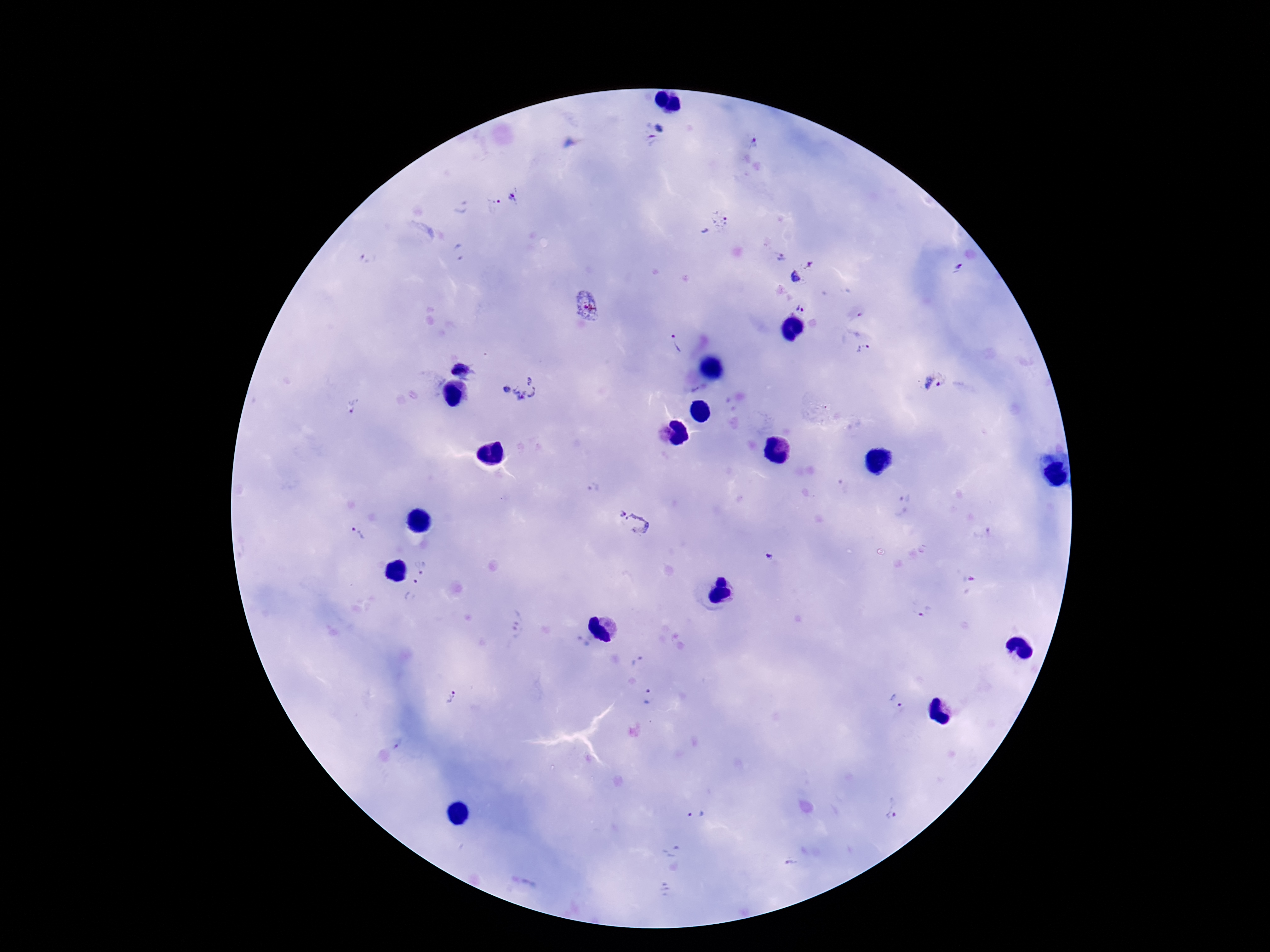
Approximate object centers, in pixels from the top-left corner.
Summary:
  - Plasmodium parasite locations: (x=658, y=128), (x=753, y=140), (x=652, y=141), (x=516, y=196), (x=493, y=204), (x=713, y=224), (x=457, y=253), (x=367, y=258), (x=781, y=258), (x=804, y=274), (x=586, y=303), (x=799, y=308), (x=675, y=344), (x=864, y=350), (x=462, y=368), (x=932, y=380), (x=518, y=388), (x=355, y=405), (x=620, y=513), (x=640, y=523), (x=358, y=535), (x=770, y=558), (x=421, y=564), (x=412, y=590), (x=924, y=611), (x=516, y=626), (x=649, y=697), (x=451, y=699), (x=895, y=700), (x=893, y=808), (x=695, y=814), (x=791, y=864)
  - Image size: 1270×952 pixels
  - Magnification: 100x
  - Patient malaria status: infected
  - Field of view: one from this slide
  - Stain: Giemsa
  - Capture: smartphone camera through the microscope eyepiece
  - Preparation: thick blood smear